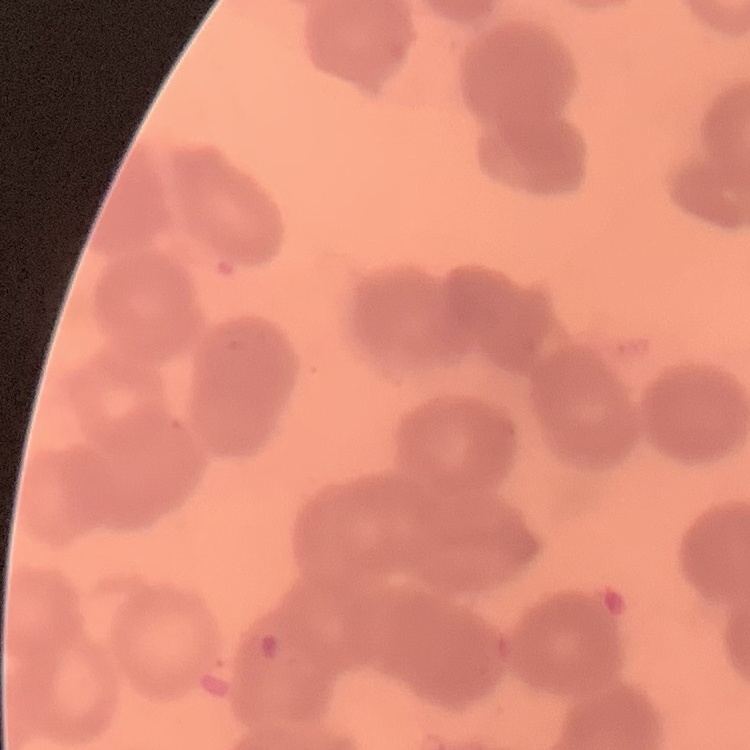

The erythrocytes show rouleaux formation. Thin peripheral smear. Field's or Giemsa stain. Square crop of a larger photomicrograph.